Assess the morphology of the red blood cells.
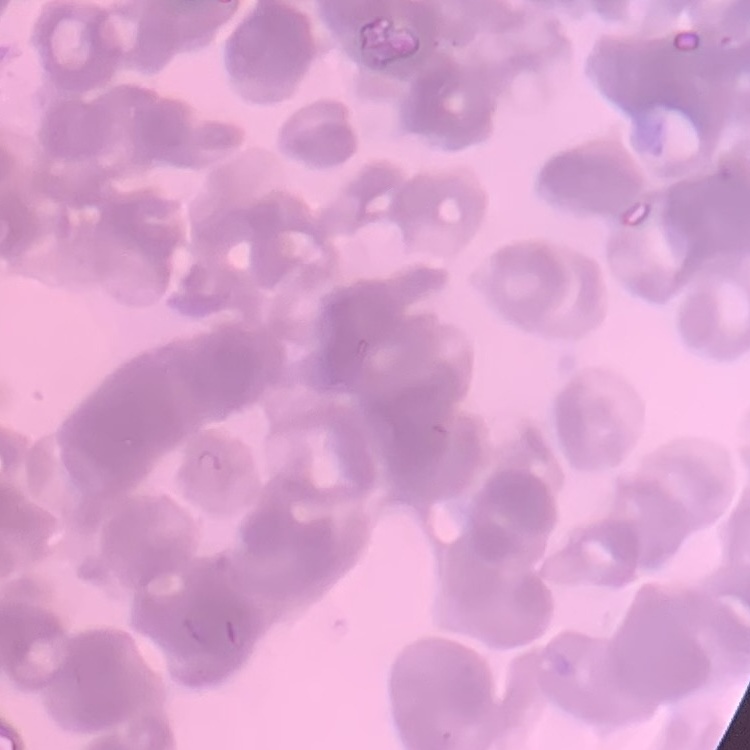
They show rouleaux formation.

Thin peripheral smear. Field's or Giemsa stain. Square crop of a larger photomicrograph.